Report the malaria status.
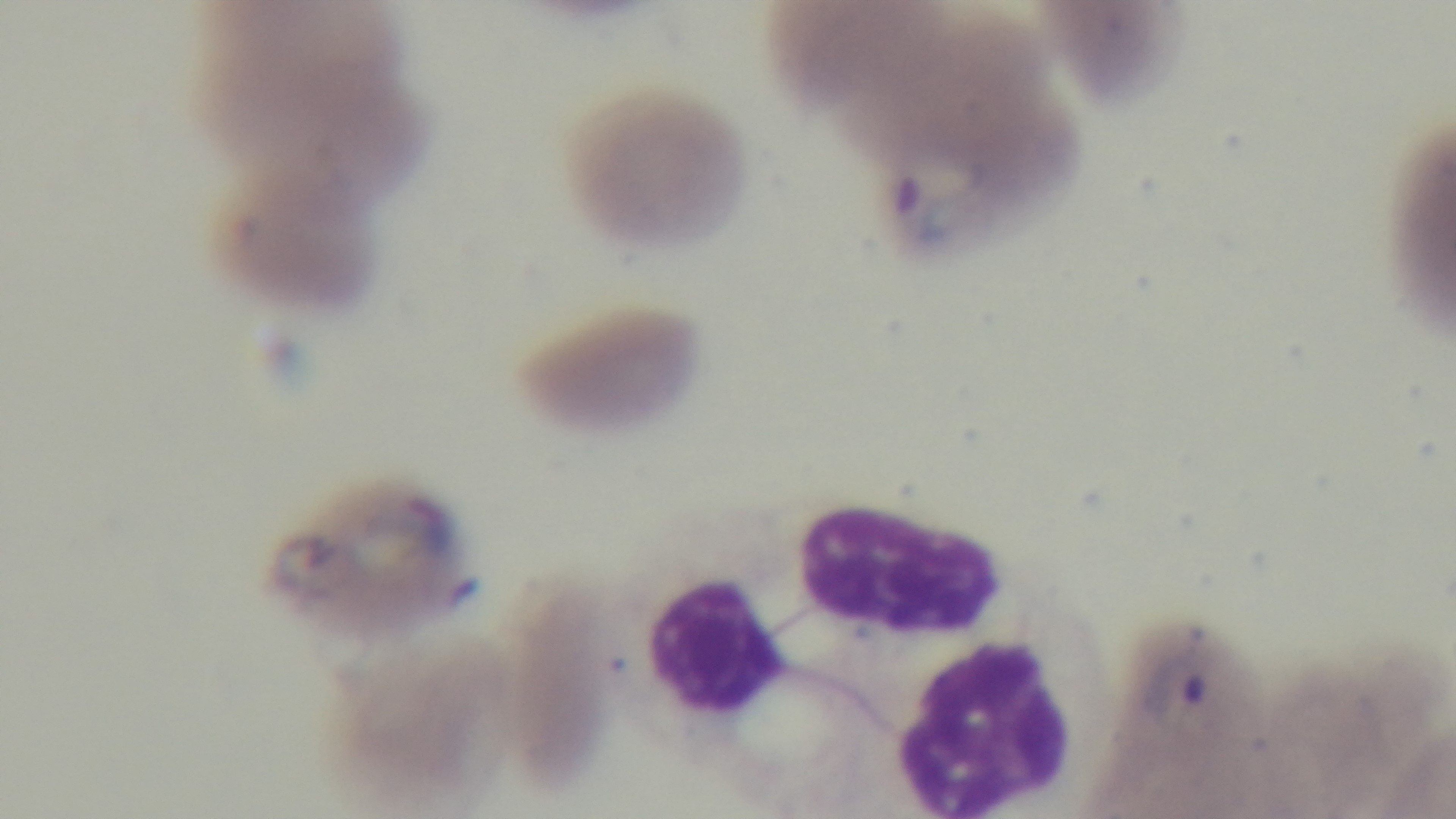

It is infected.

Summary:
  - Field of view: single
  - Preparation: thin blood film
  - Stain: Giemsa
  - Capture: mounted 4K digital camera
  - Modality: light microscopy
  - Objective: 100x oil immersion